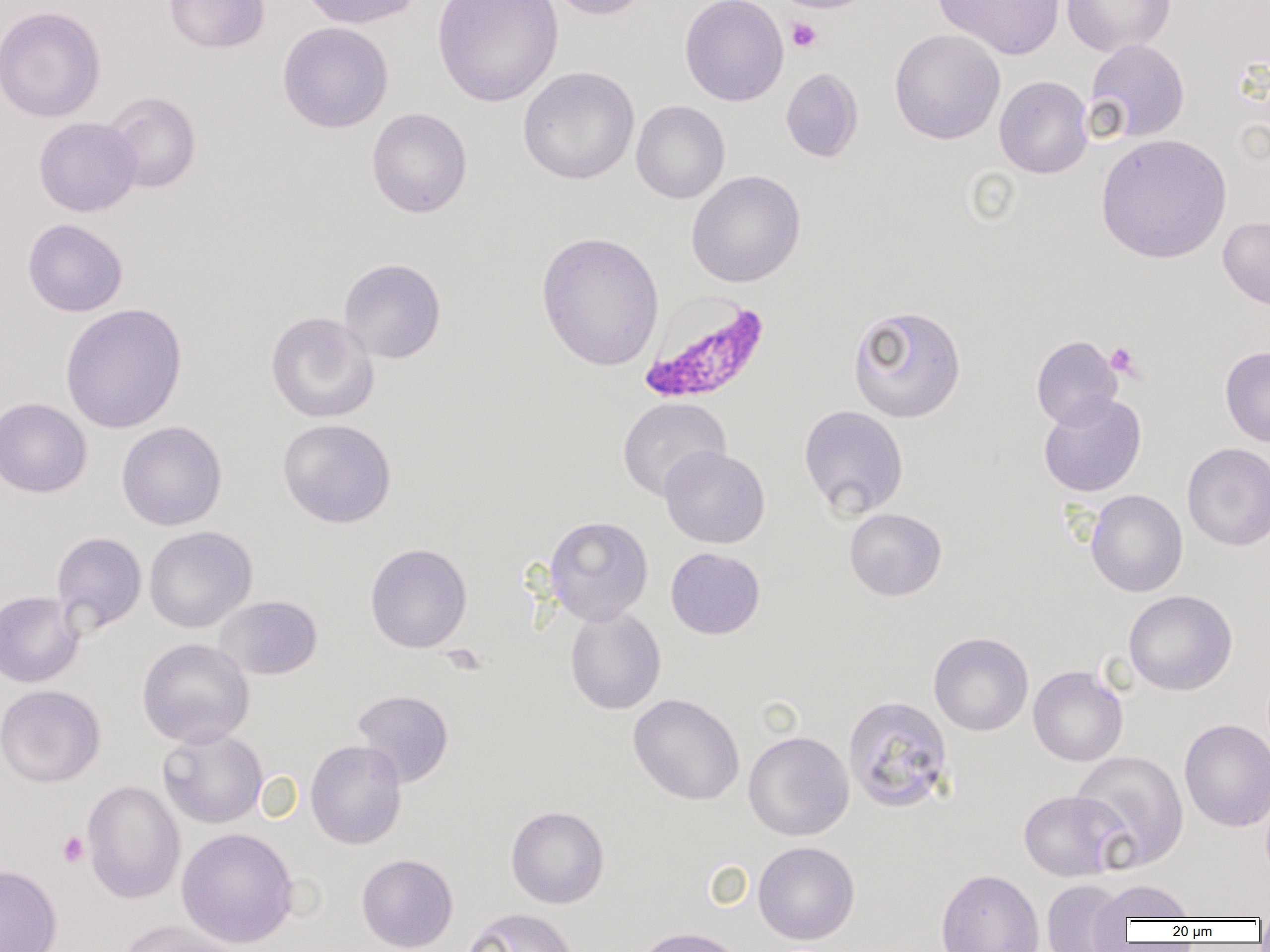
Summary:
  - Coordinate format: approximate bounding boxes as [x1, y1, x2, y2] in pixels
  - Platelet locations: [786, 17, 822, 52], [1106, 342, 1142, 379], [57, 831, 89, 867]
  - Plasmodium falciparum-infected red blood cell locations: [639, 290, 770, 405]
  - Uninfected red blood cell locations: [164, 0, 270, 53], [300, 0, 423, 29], [432, 0, 564, 107], [547, 0, 652, 20], [680, 0, 788, 107], [771, 0, 876, 13], [933, 0, 1065, 60], [1062, 0, 1176, 57], [0, 5, 106, 123], [277, 21, 394, 134], [889, 28, 1006, 145], [1084, 39, 1190, 143], [518, 66, 639, 185], [780, 67, 863, 163], [994, 75, 1093, 178], [101, 91, 202, 194], [631, 100, 730, 203], [366, 107, 472, 218], [33, 117, 142, 217], [1095, 133, 1232, 264], [686, 170, 806, 288], [1218, 216, 1270, 310], [22, 218, 128, 317], [536, 231, 664, 371], [338, 257, 446, 363], [60, 303, 188, 434], [847, 304, 967, 423], [265, 311, 379, 423], [1032, 335, 1122, 429], [1220, 345, 1270, 448], [1038, 392, 1146, 497], [0, 397, 92, 498], [617, 397, 731, 502], [798, 405, 909, 519], [277, 418, 396, 528], [116, 421, 227, 531], [1182, 442, 1270, 550], [659, 445, 769, 548], [1085, 490, 1187, 597], [844, 508, 946, 600], [545, 516, 653, 625], [144, 526, 257, 633], [51, 531, 147, 635], [365, 542, 472, 653], [666, 547, 765, 639], [1123, 589, 1237, 695], [0, 590, 85, 688], [215, 595, 322, 679], [565, 606, 666, 714], [929, 632, 1033, 736], [136, 638, 255, 748], [1028, 665, 1128, 766], [0, 684, 105, 787], [352, 690, 454, 788], [628, 694, 744, 805], [843, 695, 954, 813], [1179, 718, 1270, 832], [157, 728, 267, 829], [743, 731, 854, 841], [306, 739, 407, 849], [1070, 750, 1189, 871], [82, 779, 185, 904], [1019, 789, 1129, 881], [506, 805, 609, 908], [176, 828, 299, 948], [753, 841, 860, 944], [356, 853, 458, 952], [0, 864, 63, 952], [936, 868, 1044, 952], [1042, 879, 1129, 952], [1092, 879, 1198, 922], [462, 907, 579, 952], [117, 920, 244, 952], [631, 926, 748, 952]
  - Slide-level diagnosis: Plasmodium falciparum
  - Modality: light microscopy
  - Field of view: single
  - Image size: 1270×952 pixels
  - Preparation: thin blood film
  - Magnification: 1000x